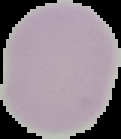
result = no Plasmodium parasites seen
preparation = thin blood smear
image type = segmented cell region with the area outside set to black
image size = 121×139 pixels